Comment on the morphology of the erythrocytes.
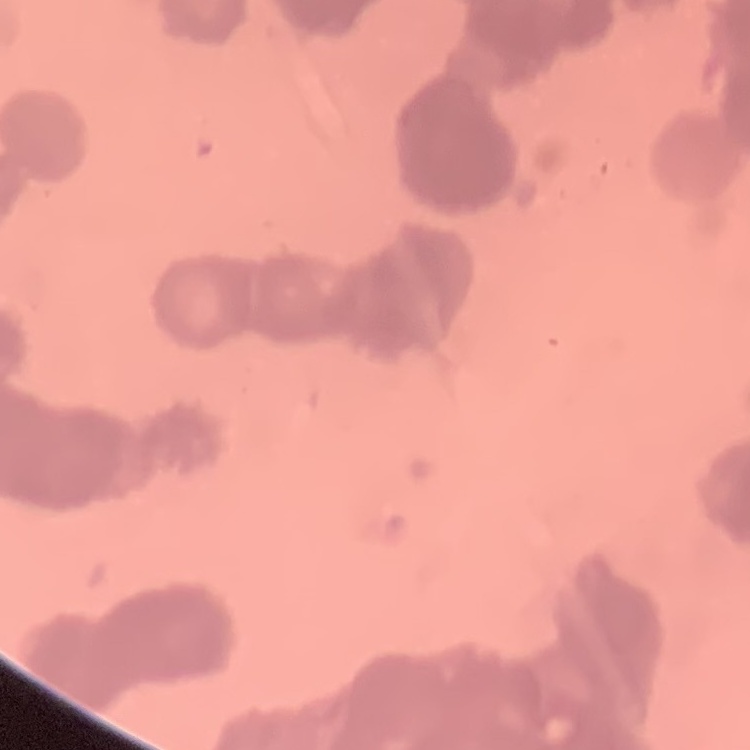
Rouleaux formation.

Square crop of a larger photomicrograph. Thin blood smear. Stained with either Field's or Giemsa.